Name the cell type shown.
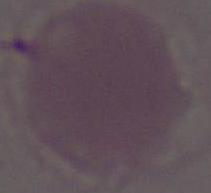

This is an erythrocyte.

magnification = 1000x
modality = photomicrograph